Locate every Plasmodium parasite.
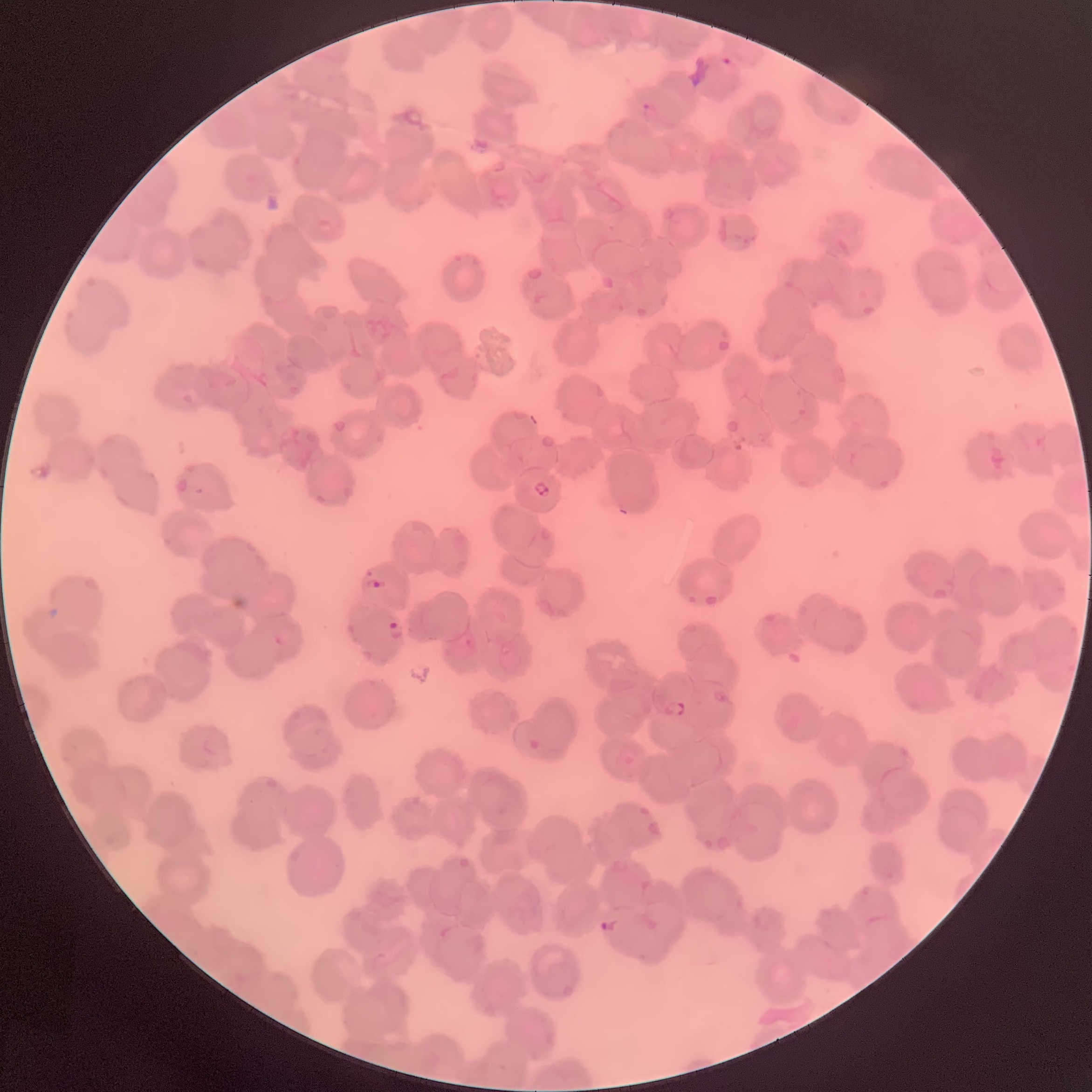
Approximate bounding boxes as [x1, y1, x2, y2] in pixels.
Plasmodium parasites: [721, 57, 734, 66], [641, 102, 659, 121], [533, 481, 550, 497], [363, 578, 386, 590], [386, 620, 405, 639], [459, 633, 476, 653], [664, 700, 686, 717], [599, 919, 621, 933].

Summary:
  - Image size: 1092×1092 pixels
  - Preparation: thin blood smear
  - Modality: optical microscopy
  - Red blood cell morphology: rouleaux formation